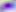

modality: photomicrograph
identification: Toxoplasma gondii
magnification: 400x